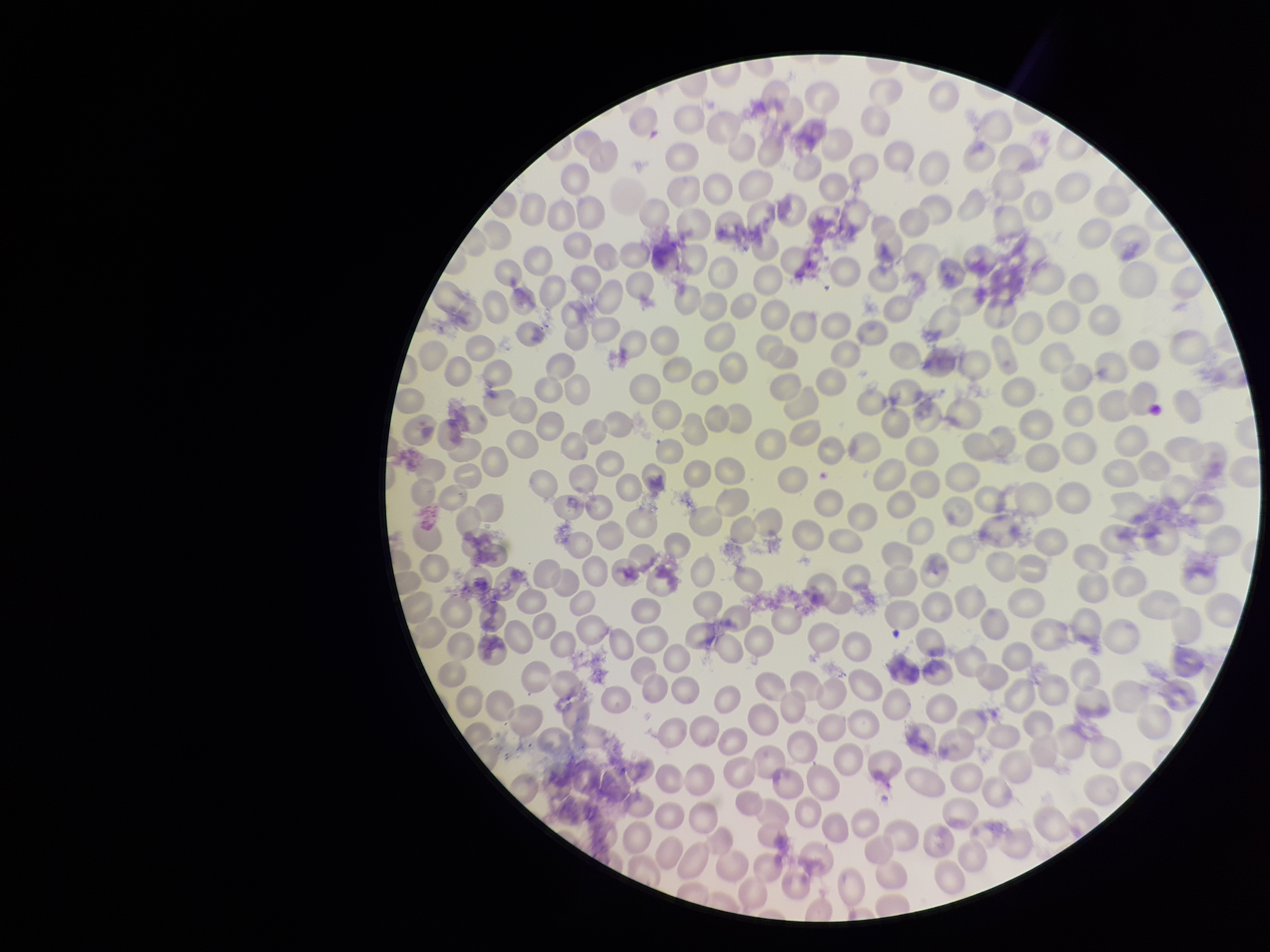

Summary:
  - Patient malaria status: infected
  - Parasitized red blood cell count: 0
  - Red blood cell count: 260
  - Preparation: thin blood smear
  - Stain: Giemsa
  - Image size: 1270×952 pixels
  - Parasitized red blood cells: none identified
  - Capture: smartphone photograph through the microscope eyepiece
  - Field of view: one from this slide
  - Species reported for this patient: Plasmodium falciparum